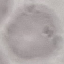
Result: negative for malaria parasites. Thin blood smear. Acquired by smartphone through the microscope eyepiece. Cell patch, automatically extracted from a larger field of view and resized to 64 × 64 pixels. Giemsa-stained preparation.